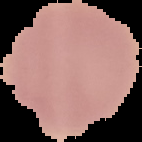
preparation = thin blood film
malaria status = uninfected
image size = 142×142 pixels
image type = segmented cell region with the area outside set to black